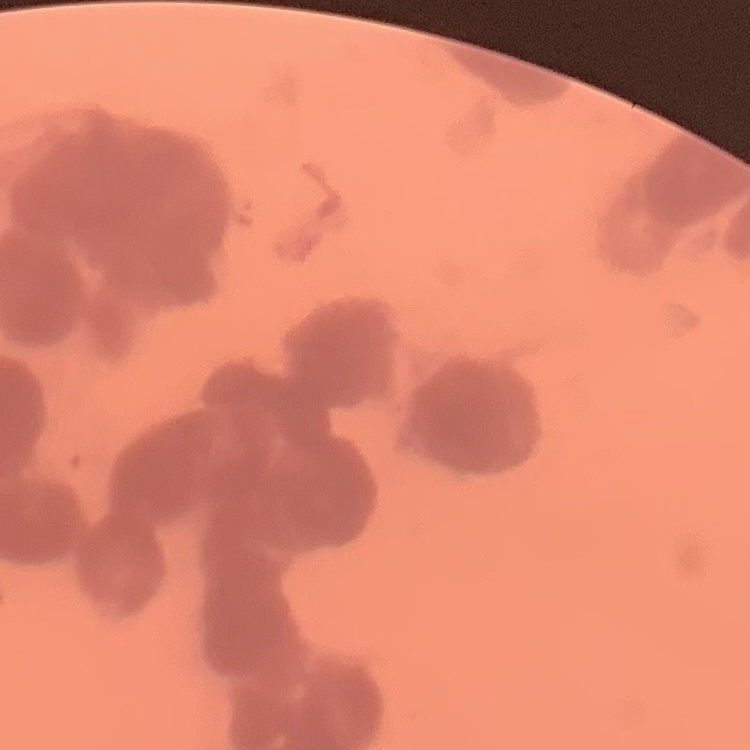 The red blood cells show rouleaux formation. Thin blood smear. One tile cut from a larger photomicrograph. Stained with either Field's or Giemsa.